Assess for malaria.
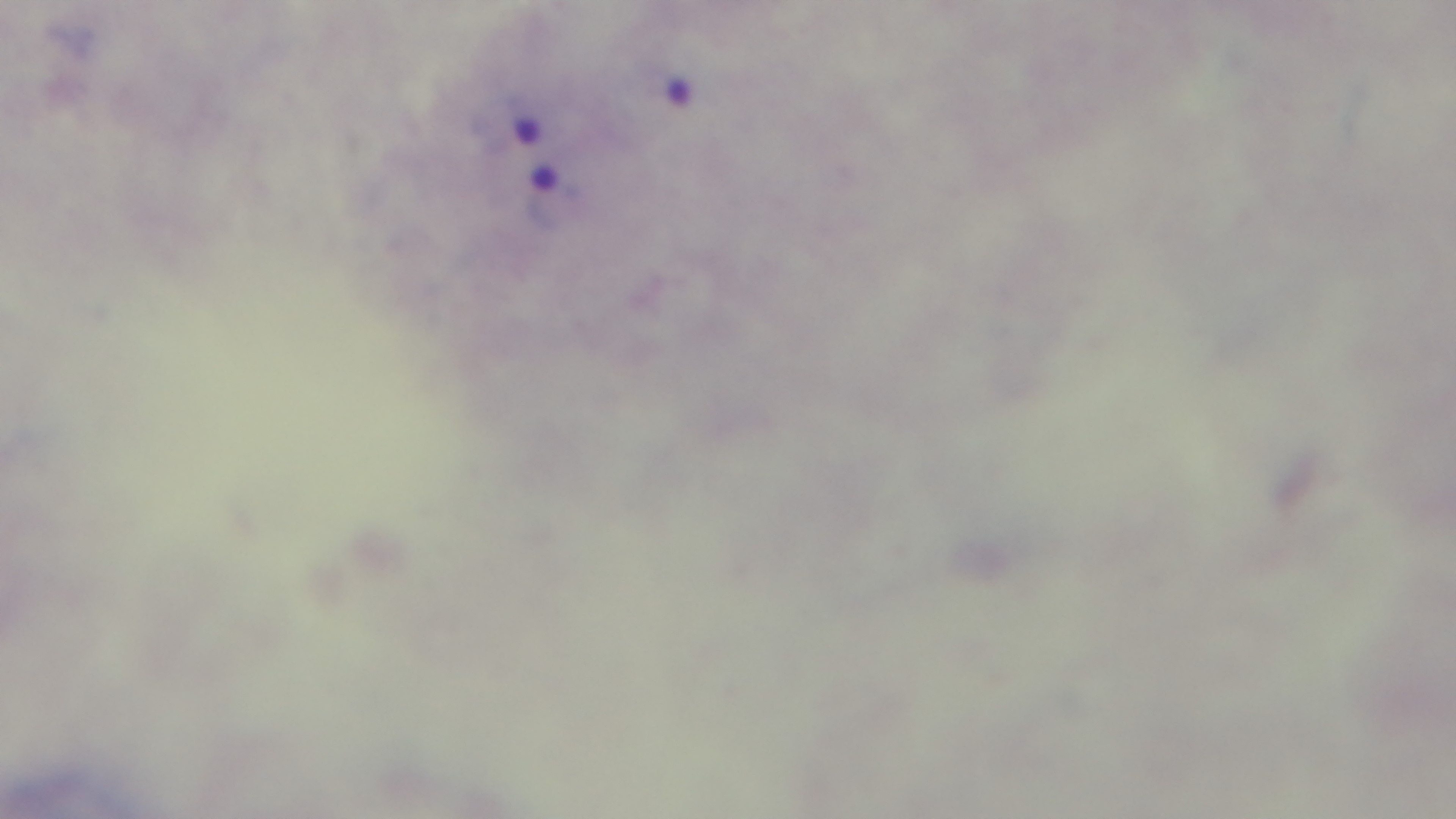

Infected.

100x oil-immersion objective. Captured with a mounted 4K digital camera. One field from the slide. Preparation: thick smear. Light microscopy. Giemsa stain.